Locate every uninfected red blood cell.
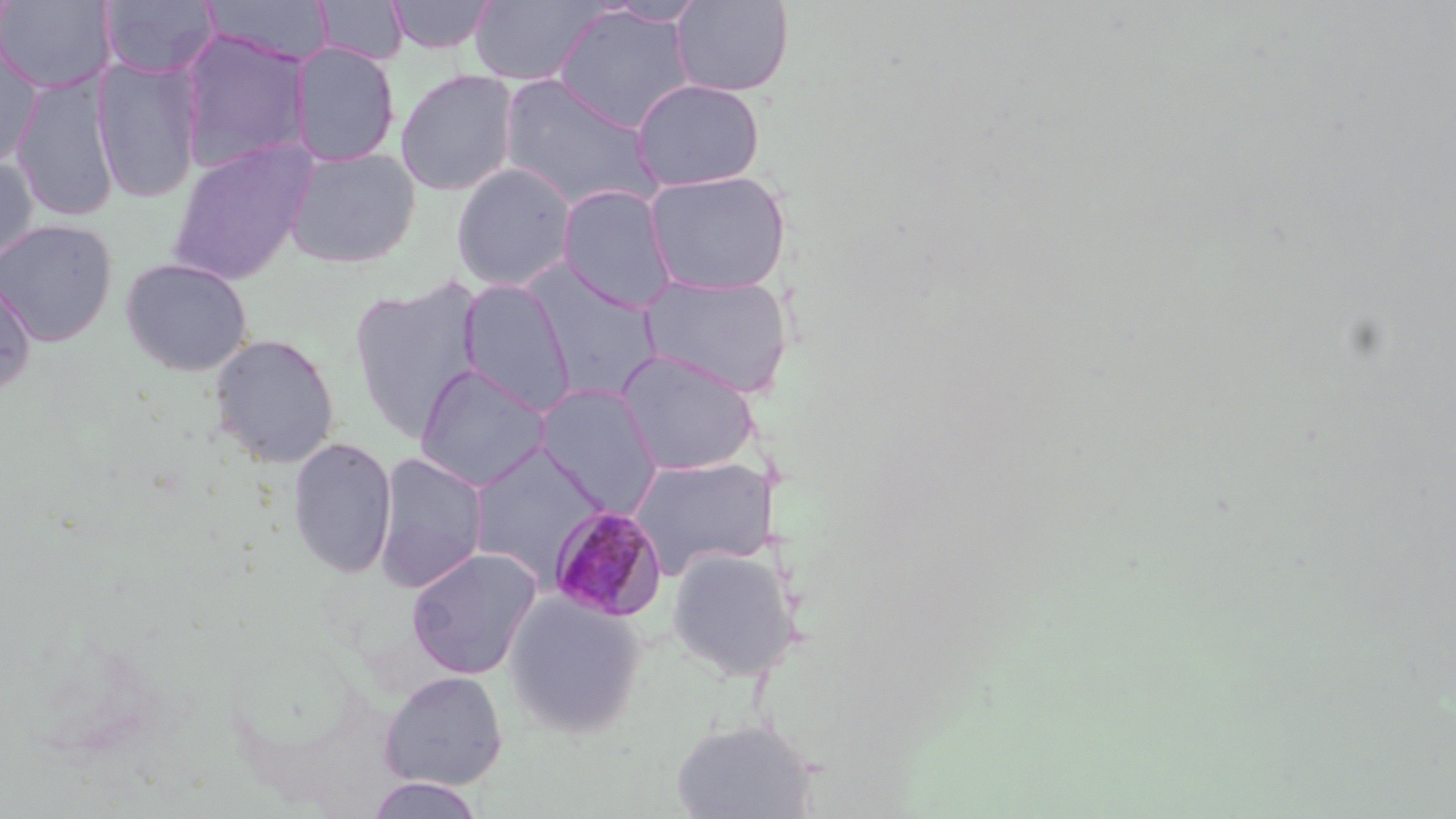

Approximate bounding boxes as (x1, y1, x2, y2) in pixels.
Uninfected red blood cells: (0, 0, 116, 95), (100, 0, 219, 78), (202, 0, 333, 65), (386, 0, 499, 55), (670, 0, 795, 97), (313, 1, 407, 65), (468, 1, 609, 86), (601, 1, 710, 27), (551, 5, 696, 134), (176, 29, 311, 175), (289, 41, 401, 167), (0, 47, 42, 171), (94, 55, 203, 205), (395, 69, 519, 196), (11, 73, 120, 223), (499, 74, 662, 213), (630, 78, 766, 191), (166, 138, 318, 286), (284, 147, 421, 268), (0, 156, 39, 272), (451, 162, 577, 292), (644, 170, 792, 295), (557, 184, 678, 312), (0, 219, 117, 347), (119, 257, 253, 376), (522, 264, 665, 404), (639, 271, 795, 398), (348, 275, 484, 441), (0, 276, 37, 394), (457, 278, 576, 416), (209, 332, 341, 468), (614, 349, 761, 475), (414, 363, 553, 492), (533, 383, 666, 518), (288, 436, 397, 579), (467, 441, 609, 585), (373, 451, 489, 593), (628, 455, 778, 578), (405, 546, 543, 679), (666, 547, 802, 681), (502, 588, 647, 739), (378, 670, 508, 790), (670, 717, 820, 819), (364, 776, 488, 818).

Summary:
  - Plasmodium malariae-infected red blood cell locations: (548, 505, 668, 622)
  - Slide-level diagnosis: Plasmodium malariae
  - Preparation: thin blood smear
  - Stain: May-Grünwald-Giemsa
  - Magnification: 1000x
  - Image size: 1456×819 pixels
  - Modality: light microscopy
  - Field of view: single